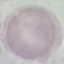
result = no malaria parasites seen
preparation = thin blood smear
image type = cell patch, automatically extracted from a larger field of view and resized to 64 × 64 pixels
stain = Giemsa
capture = smartphone through the microscope eyepiece